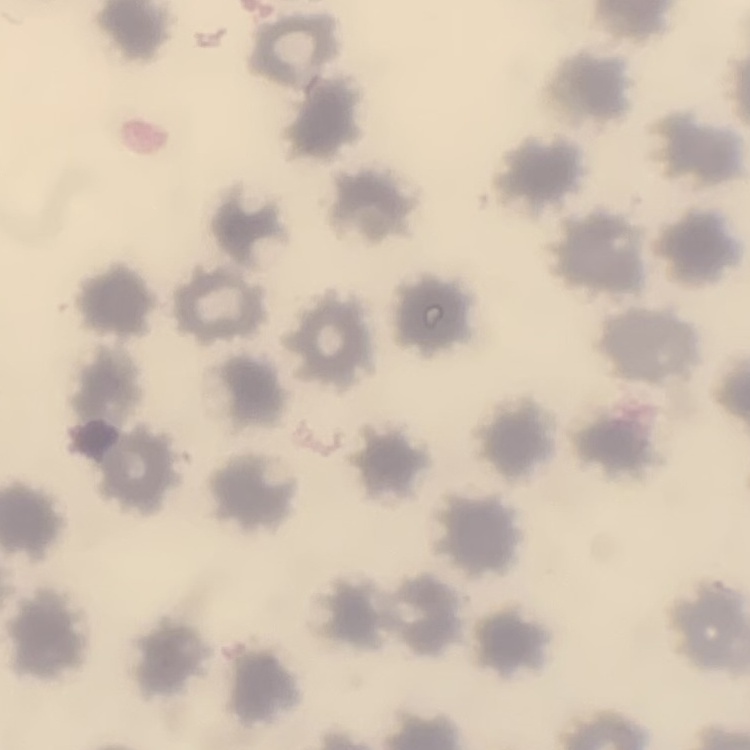
The red blood cells exhibit no rouleaux formation. One tile cut from a larger photomicrograph. Stained with either Field's or Giemsa. Thin peripheral smear.